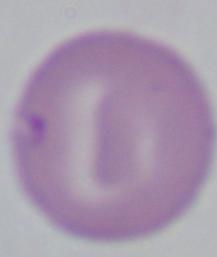

Summary:
  - Identification: Babesia
  - Magnification: 1000x
  - Modality: photomicrograph